Give the position of each P. falciparum parasite with its life-cycle stage, each leukocyte, and any debris.
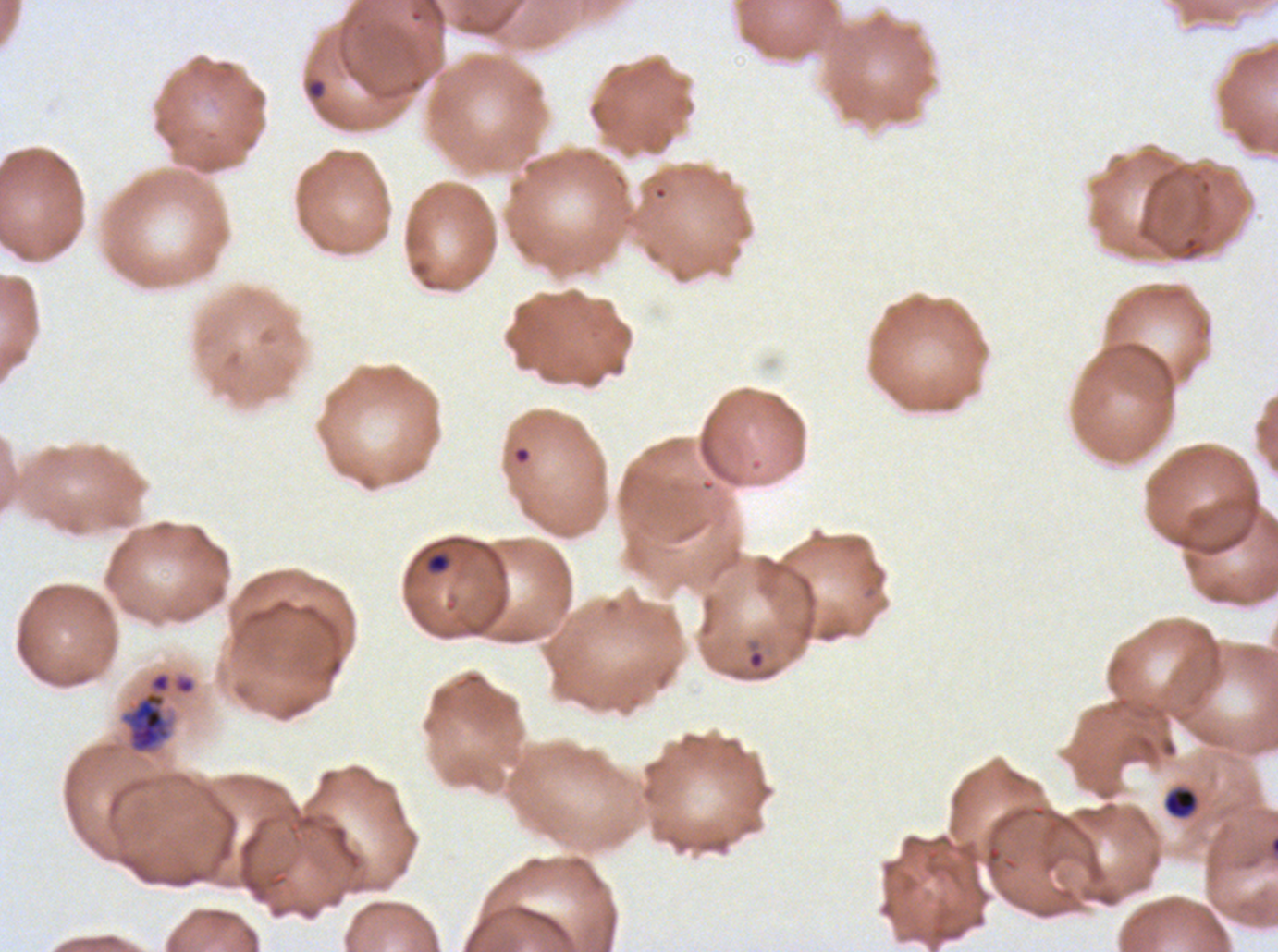
Approximate bounding boxes as {x1, y1, x2, y2} in pixels.
Rings: {746, 649, 765, 670}.
Late-ring/early-trophozoite forms: {1163, 787, 1198, 819}.
Late trophozoites: {117, 669, 198, 757}.
Debris: {306, 78, 326, 100}, {425, 551, 450, 574}.
No mid trophozoites, early schizonts, late schizonts, segmenters, gametocytes, or leukocytes observed.

{
  "stain": "Giemsa",
  "preparation": "thin blood film",
  "life_cycle_stages_observed": "ring, late-ring/early-trophozoite, late trophozoite",
  "specimen": "ex-vivo P. falciparum culture from a patient in The Gambia, grown for 24 to 48 hours",
  "field_of_view": "one sub-image of a larger composite",
  "image_size": "1278×952 pixels"
}